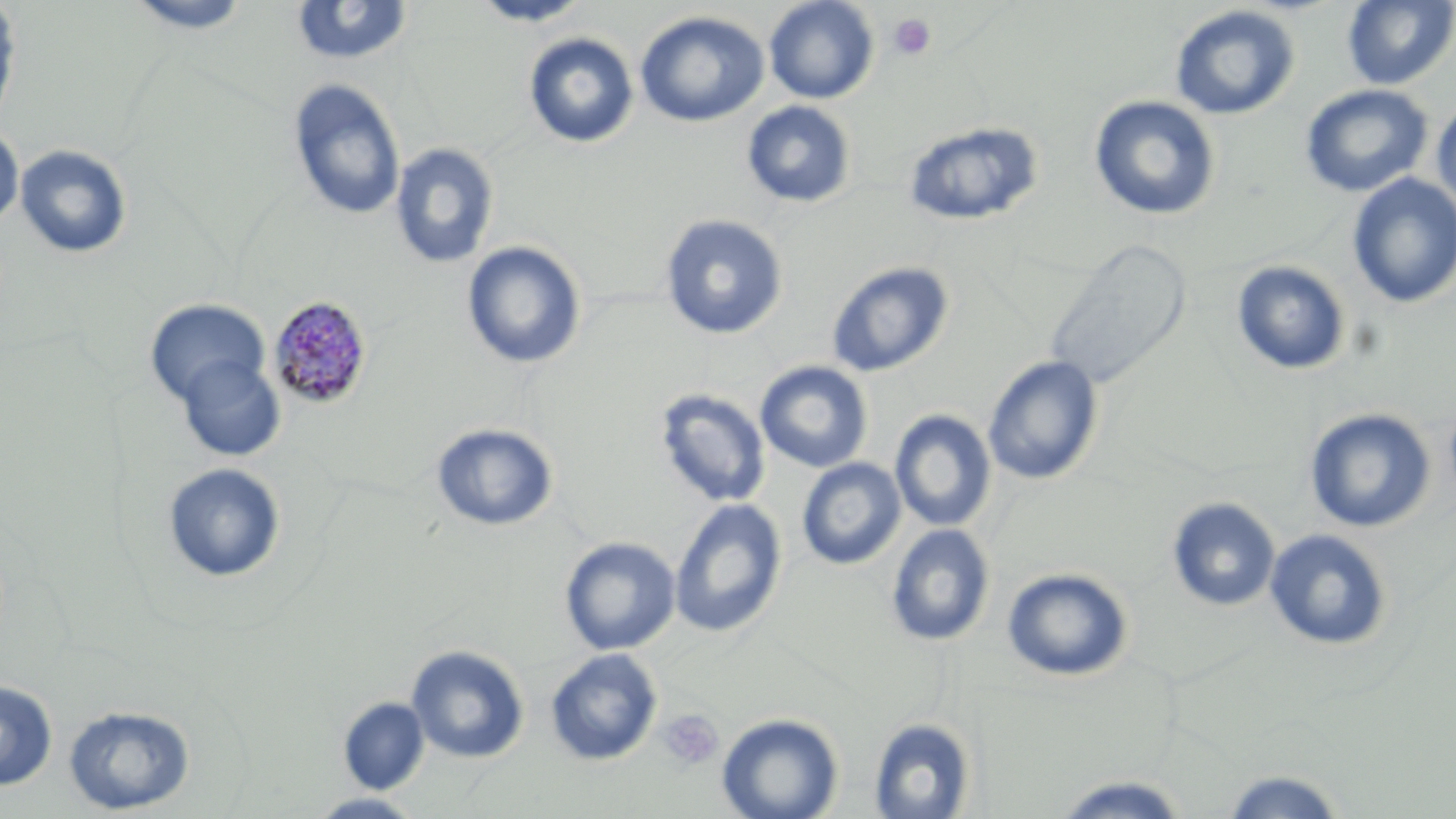
Summary:
  - Coordinate format: approximate bounding boxes as [x1, y1, x2, y2] in pixels
  - Platelet locations: [888, 13, 935, 60], [658, 708, 724, 771]
  - Uninfected red blood cell locations (subset): [123, 0, 255, 34], [468, 0, 593, 26], [763, 0, 880, 104], [1342, 0, 1456, 90], [0, 1, 23, 133], [289, 2, 415, 67], [1169, 5, 1301, 120], [635, 10, 770, 128], [522, 32, 639, 149], [287, 78, 406, 221], [1300, 84, 1433, 197], [1088, 95, 1222, 220], [1431, 97, 1456, 214], [741, 100, 856, 208], [902, 121, 1044, 226], [0, 122, 24, 232], [389, 142, 500, 270], [14, 144, 133, 259], [1347, 173, 1456, 308], [660, 214, 788, 340], [1043, 238, 1193, 391], [462, 241, 586, 369], [1230, 260, 1351, 376], [826, 261, 955, 377], [144, 298, 270, 409], [982, 355, 1104, 486], [174, 357, 286, 462], [755, 361, 873, 472], [654, 389, 771, 507], [1304, 407, 1437, 533], [889, 409, 997, 532], [431, 422, 558, 532], [796, 458, 906, 570], [162, 463, 286, 584], [1166, 496, 1281, 612], [669, 498, 787, 639], [885, 523, 995, 647], [1264, 529, 1393, 651], [559, 536, 681, 655], [1001, 567, 1135, 682], [406, 644, 530, 763], [545, 648, 663, 766], [0, 680, 58, 790], [338, 697, 429, 794], [63, 704, 195, 815], [717, 712, 844, 819], [869, 717, 975, 818], [1217, 768, 1349, 818], [1049, 774, 1195, 817], [305, 792, 427, 818]
  - Slide-level diagnosis: Plasmodium malariae
  - Image size: 1456×819 pixels
  - Stain: May-Grünwald-Giemsa
  - Magnification: 1000x
  - Field of view: one of a larger specimen
  - Modality: light microscopy
  - Preparation: thin blood smear